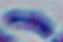

{
  "magnification": "1000x",
  "identification": "Toxoplasma gondii",
  "modality": "micrograph"
}